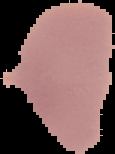

Image is 115×154 pixels. Result: negative for malaria parasites. From a thin blood smear. Segmented cell region on a black background.